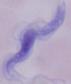
magnification = 1000x
identification = trypanosome
modality = micrograph